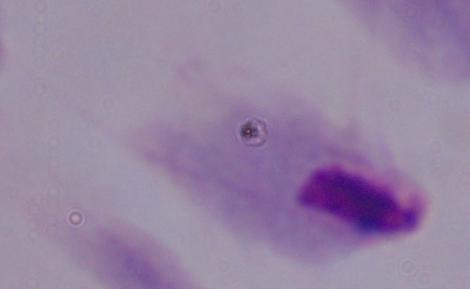
magnification = 1000x
identification = trichomonad
modality = photomicrograph